Assess this cell for malaria.
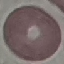

Uninfected.

image type = cell patch, automatically extracted from a larger field of view and resized to 64 × 64 pixels
stain = Giemsa
preparation = thin blood smear
capture = smartphone camera at the microscope eyepiece